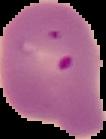
{
  "image_type": "segmented cell region on a black background",
  "image_size": "106×139 pixels",
  "preparation": "thin blood smear",
  "malaria_status": "parasitized"
}